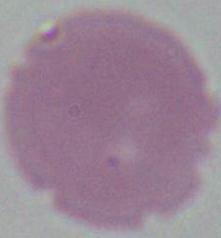

Summary:
  - Magnification: 1000x
  - Identification: erythrocyte
  - Modality: photomicrograph